Outline each blood parasite and name the species.
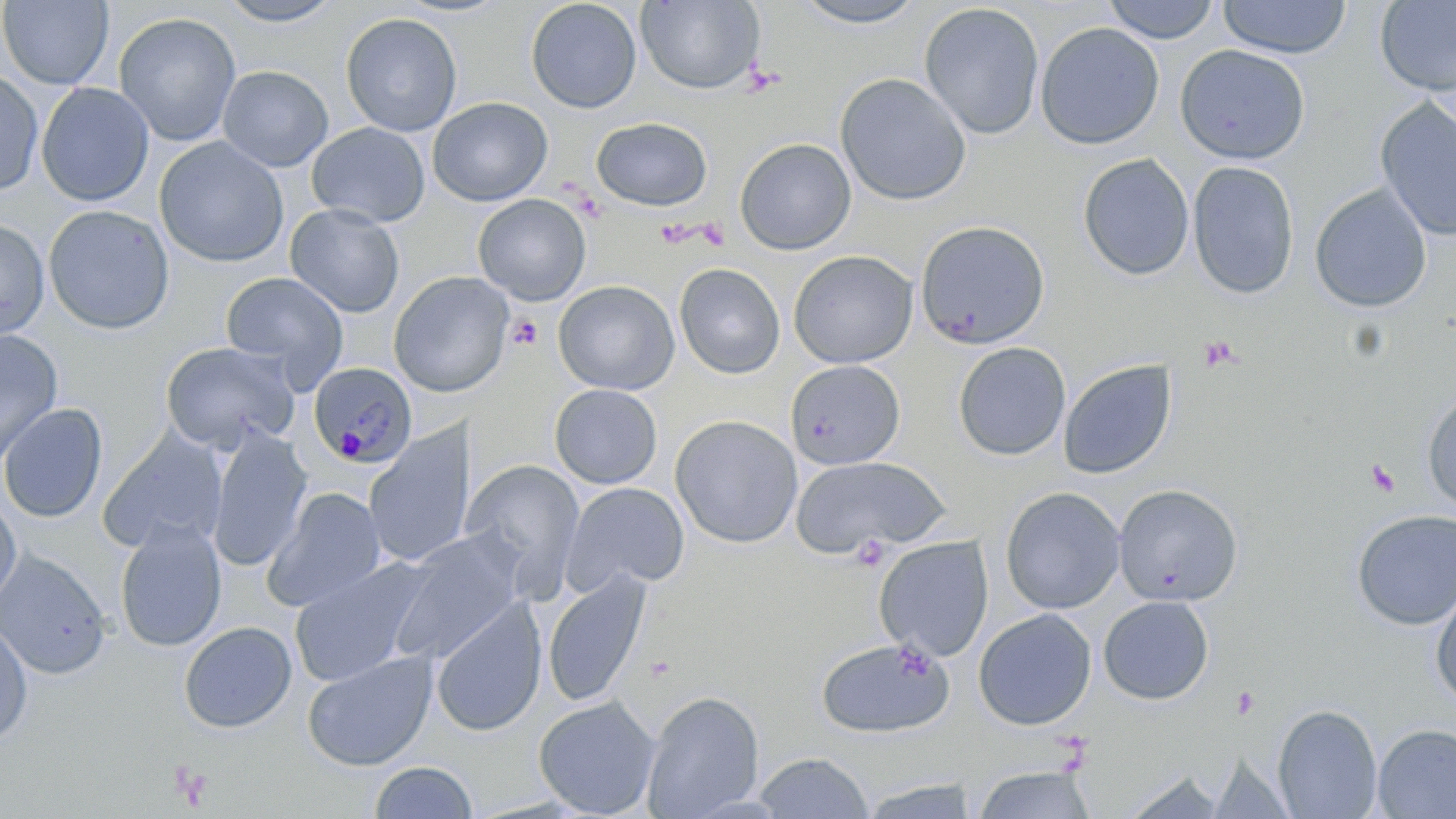
Approximate bounding boxes as (x1,y1)-(x2,y2) corner pairs in pixels.
Plasmodium malariae-infected red blood cells: (308,361)-(417,468).
No Plasmodium falciparum, Plasmodium ovale, Plasmodium vivax, Babesia divergens, or Trypanosoma brucei observed.

slide-level diagnosis = Plasmodium malariae
stain = May-Grünwald-Giemsa
field of view = one of a larger specimen
preparation = thin blood smear
magnification = 1000x
uninfected red blood cell locations = approximate bounding boxes as (x1,y1)-(x2,y2) corner pairs in pixels: (0,0)-(114,90), (389,0)-(515,18), (525,0)-(642,114), (788,0)-(930,29), (1103,0)-(1220,44), (1218,0)-(1351,59), (1375,0)-(1456,98), (215,1)-(345,27), (636,1)-(765,94), (919,3)-(1045,140), (114,12)-(241,146), (340,12)-(463,137), (1035,22)-(1165,150), (1174,44)-(1311,165), (217,65)-(333,172), (0,68)-(44,196), (834,72)-(972,206), (36,82)-(155,206), (1374,96)-(1456,242), (428,97)-(553,207), (592,116)-(713,211), (306,122)-(430,228), (153,137)-(289,268), (735,137)-(856,255), (1078,153)-(1195,281), (1187,161)-(1300,299), (1310,183)-(1432,313), (472,193)-(592,306), (285,203)-(405,318), (43,204)-(175,334), (0,219)-(49,340), (914,220)-(1051,349), (788,250)-(919,368), (674,263)-(785,379), (388,271)-(514,398), (220,272)-(349,390), (553,280)-(680,395), (0,329)-(63,464), (160,341)-(301,453), (953,342)-(1071,461), (1058,359)-(1177,480), (785,360)-(906,470), (549,384)-(662,488), (1422,388)-(1456,516), (0,402)-(107,523), (670,415)-(803,549), (363,423)-(478,569), (207,427)-(313,572), (99,429)-(227,554), (791,455)-(949,558), (461,458)-(586,593), (561,482)-(690,597), (1112,484)-(1243,606), (263,487)-(386,612), (1000,487)-(1125,615), (0,497)-(22,610), (1351,508)-(1456,631), (114,519)-(227,653), (391,531)-(527,663), (874,536)-(993,661), (0,551)-(111,678), (288,557)-(435,687), (542,570)-(651,708), (1430,581)-(1456,710), (1098,595)-(1214,705), (430,596)-(547,738), (974,608)-(1097,730), (0,619)-(34,745), (178,620)-(297,733), (816,637)-(955,738), (301,651)-(437,771), (641,690)-(764,818), (533,696)-(661,818), (1273,704)-(1382,818), (1372,723)-(1456,818), (753,752)-(874,818), (369,761)-(477,818), (973,765)-(1097,818), (1122,770)-(1226,818), (854,776)-(982,818)
platelet locations = approximate bounding boxes as (x1,y1)-(x2,y2) corner pairs in pixels: (507,315)-(543,350), (1199,336)-(1240,371), (1364,458)-(1401,496), (169,763)-(211,808)
modality = light microscopy
image size = 1456×819 pixels